Assess the morphology of the erythrocytes.
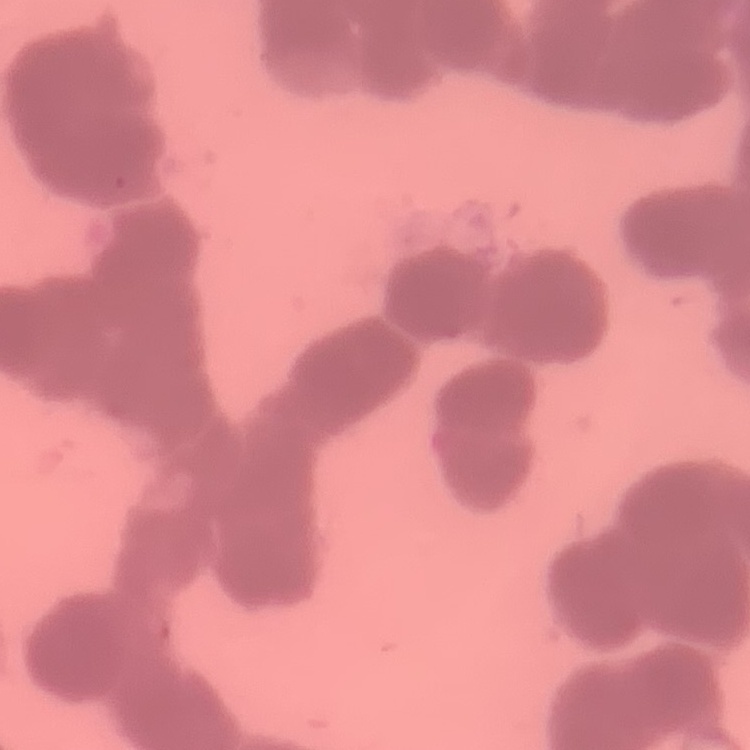

They show rouleaux formation.

{
  "preparation": "thin peripheral smear",
  "stain": "Field's or Giemsa",
  "image_type": "square crop of a larger photomicrograph"
}